Assess this cell for malaria.
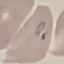
It is parasitized.

preparation = thin blood film
image type = automatically extracted cell patch, resized to 64 × 64 pixels
stain = Giemsa
capture = smartphone through the microscope eyepiece